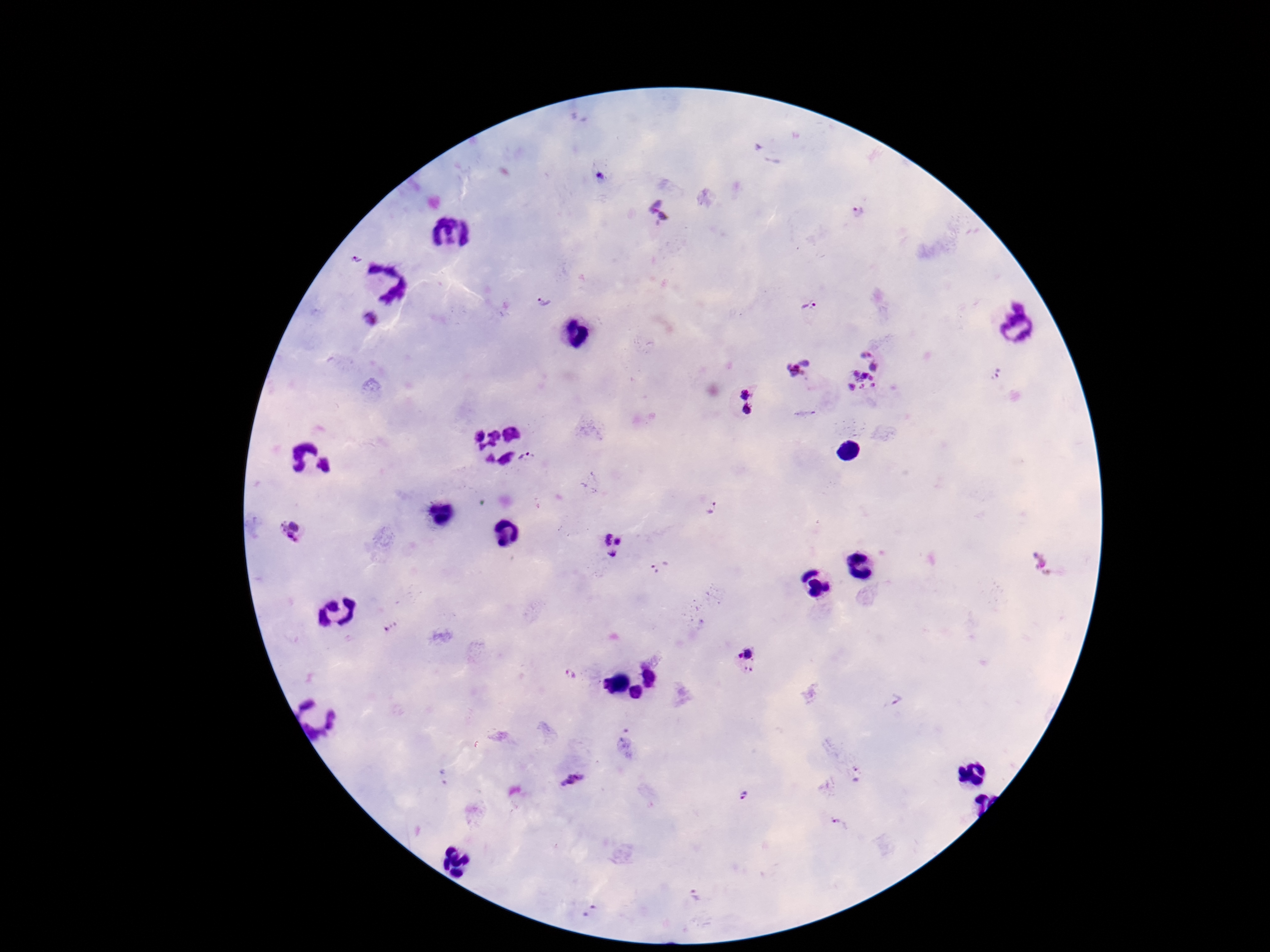

Approximate centers as (x, y) in pixels.
Summary:
  - Plasmodium parasite locations: (601, 177), (857, 211), (659, 212), (357, 258), (542, 300), (809, 304), (370, 321), (798, 367), (863, 374), (745, 393), (748, 410), (529, 458), (712, 508), (292, 529), (610, 545), (658, 567), (390, 626), (748, 661), (571, 676), (895, 701), (857, 775), (572, 781), (745, 794), (838, 824), (694, 894)
  - Patient malaria status: infected
  - Magnification: 100x
  - Preparation: thick peripheral-blood smear
  - Capture: smartphone camera through the microscope eyepiece
  - Field of view: one from this slide
  - Stain: Giemsa
  - Image size: 1270×952 pixels